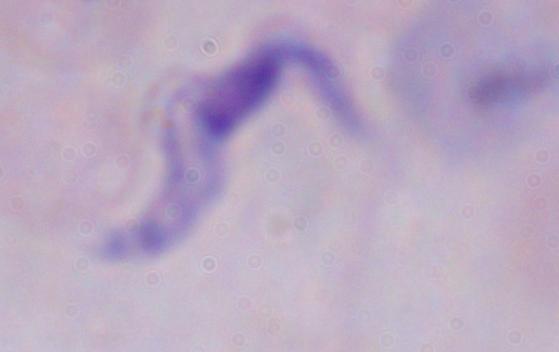
A trypanosome is shown. 1000x magnification. Photomicrograph.